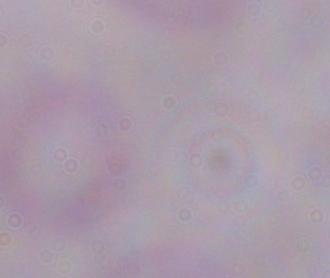
Summary:
  - Identification: trypanosome
  - Magnification: 1000x
  - Modality: photomicrograph